Describe the morphology of the red blood cells.
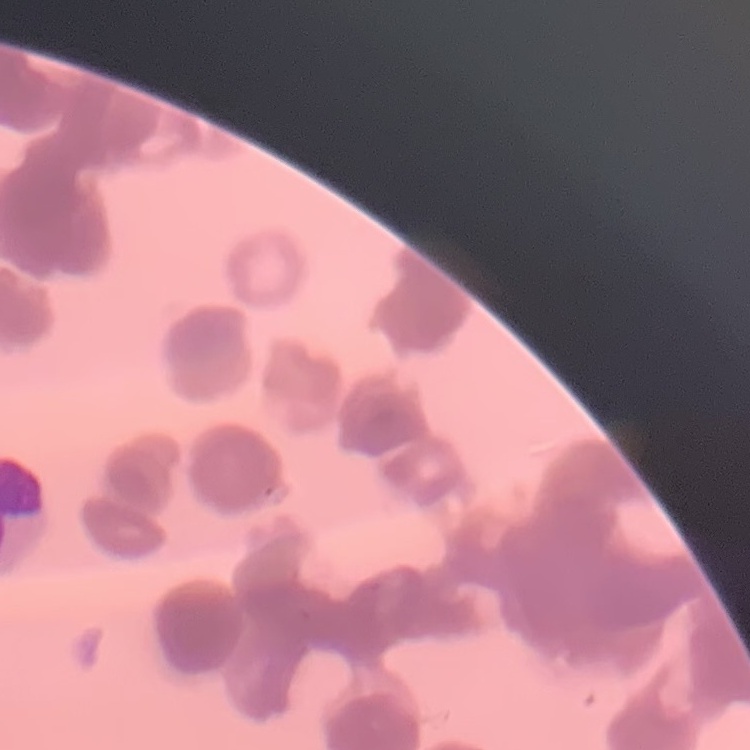

They show rouleaux formation.

image type = square crop of a larger photomicrograph
stain = Field's or Giemsa
preparation = thin blood film